Describe the morphology of the erythrocytes.
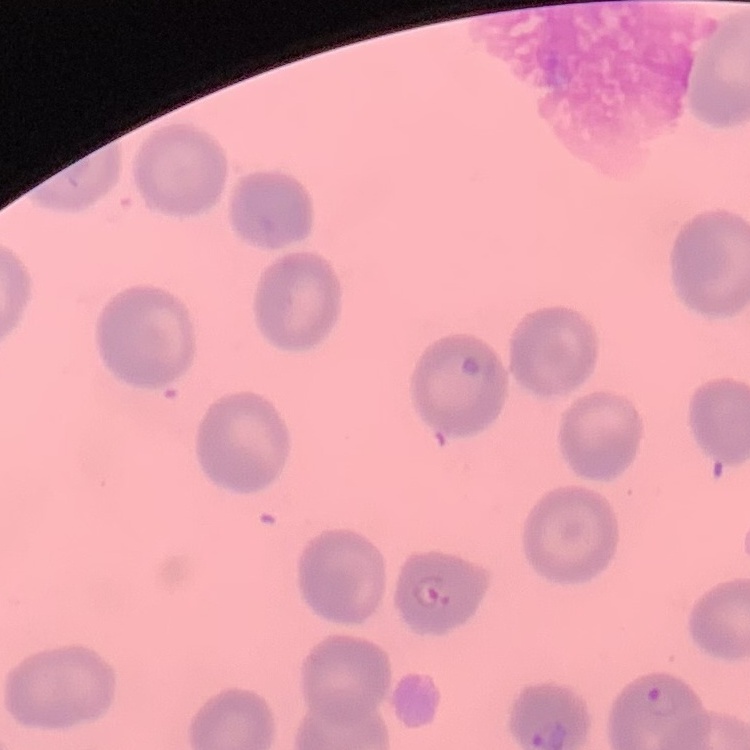

They show no rouleaux formation.

Summary:
  - Stain: Field's or Giemsa
  - Image type: square crop of a larger photomicrograph
  - Preparation: thin blood film